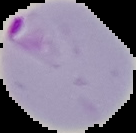

From a thin blood film. Cell region segmented out of the field of view; the surrounding area is masked to black. Malaria status: parasitized. Image is 136×133 pixels.